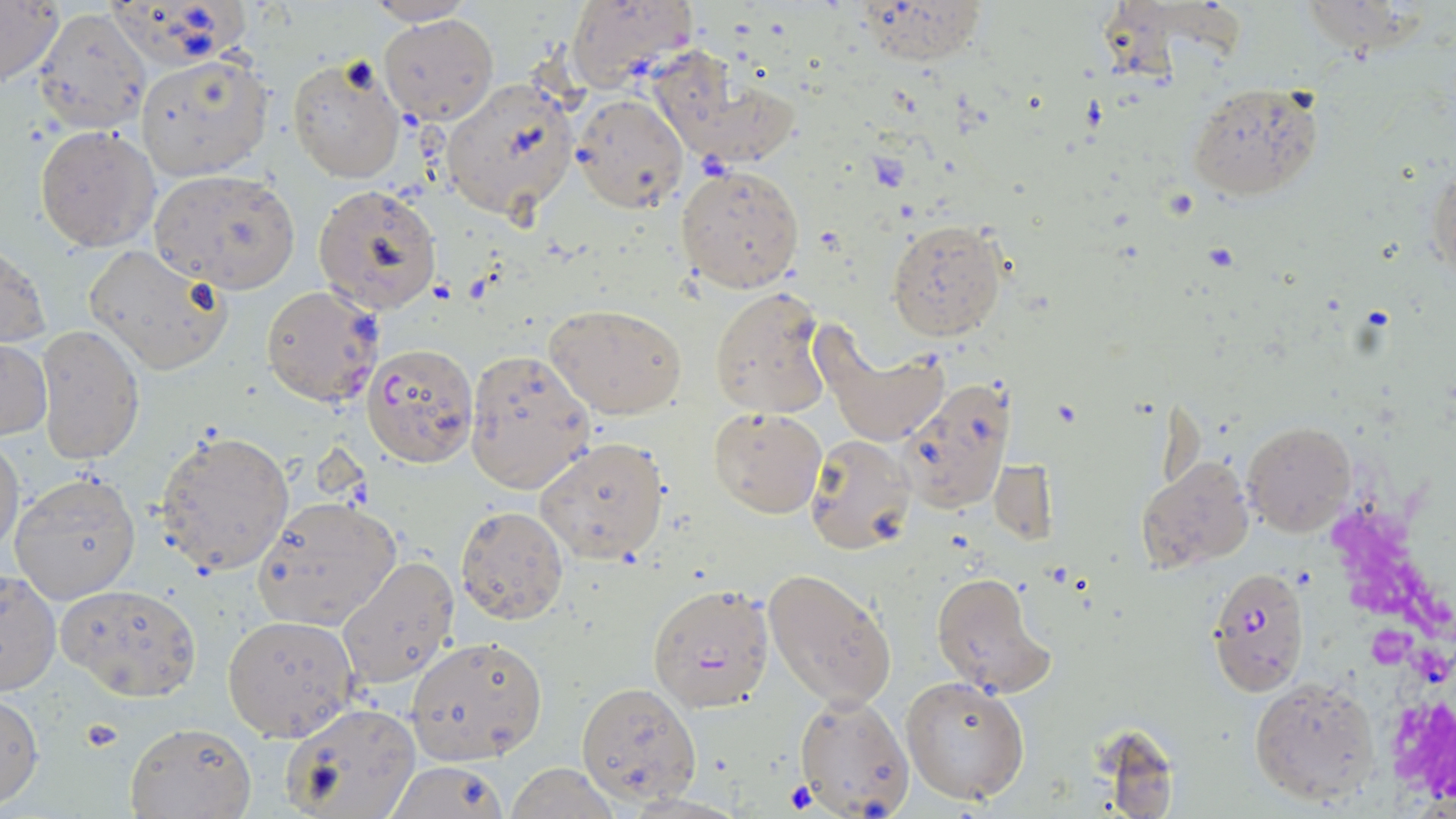

slide-level diagnosis = Plasmodium falciparum
uninfected red blood cell locations = approximate bounding boxes as [x1, y1, x2, y2] in pixels: [362, 0, 478, 25], [565, 0, 696, 93], [850, 0, 988, 67], [1, 1, 62, 88], [31, 7, 151, 132], [379, 14, 498, 124], [649, 47, 802, 171], [135, 53, 273, 181], [286, 55, 406, 183], [440, 77, 578, 219], [1187, 83, 1323, 201], [568, 92, 688, 214], [35, 125, 159, 251], [674, 162, 805, 293], [1429, 165, 1455, 280], [147, 168, 300, 294], [312, 184, 442, 313], [886, 218, 1006, 341], [1, 241, 50, 352], [85, 243, 232, 376], [709, 285, 833, 420], [546, 304, 687, 420], [813, 321, 948, 449], [36, 326, 143, 464], [0, 340, 51, 440], [464, 347, 596, 492], [898, 377, 1015, 514], [708, 406, 827, 518], [1245, 420, 1356, 537], [155, 429, 296, 577], [0, 435, 24, 560], [535, 435, 669, 564], [804, 436, 915, 554], [1136, 454, 1254, 574], [990, 458, 1057, 545], [9, 470, 141, 604], [251, 497, 402, 632], [455, 505, 569, 624], [336, 554, 458, 690], [760, 568, 899, 711], [1, 570, 60, 696], [929, 571, 1055, 696], [56, 580, 202, 700], [646, 583, 775, 712], [222, 615, 359, 741], [405, 635, 548, 763], [899, 675, 1031, 805], [1249, 676, 1381, 805], [577, 681, 702, 804], [792, 691, 914, 818], [0, 692, 45, 807], [281, 701, 420, 819], [123, 720, 256, 818], [384, 759, 510, 819], [504, 764, 622, 819]
platelet locations = approximate bounding boxes as [x1, y1, x2, y2] in pixels: [77, 718, 124, 756]
magnification = 1000x
preparation = thin blood film
field of view = single
stain = May-Grünwald-Giemsa
modality = light microscopy
Plasmodium falciparum-infected red blood cell locations = approximate bounding boxes as [x1, y1, x2, y2] in pixels: [261, 284, 381, 407], [361, 343, 478, 467], [1207, 566, 1308, 693]
image size = 1456×819 pixels